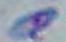 Toxoplasma gondii is seen. Micrograph. Captured at 1000x magnification.